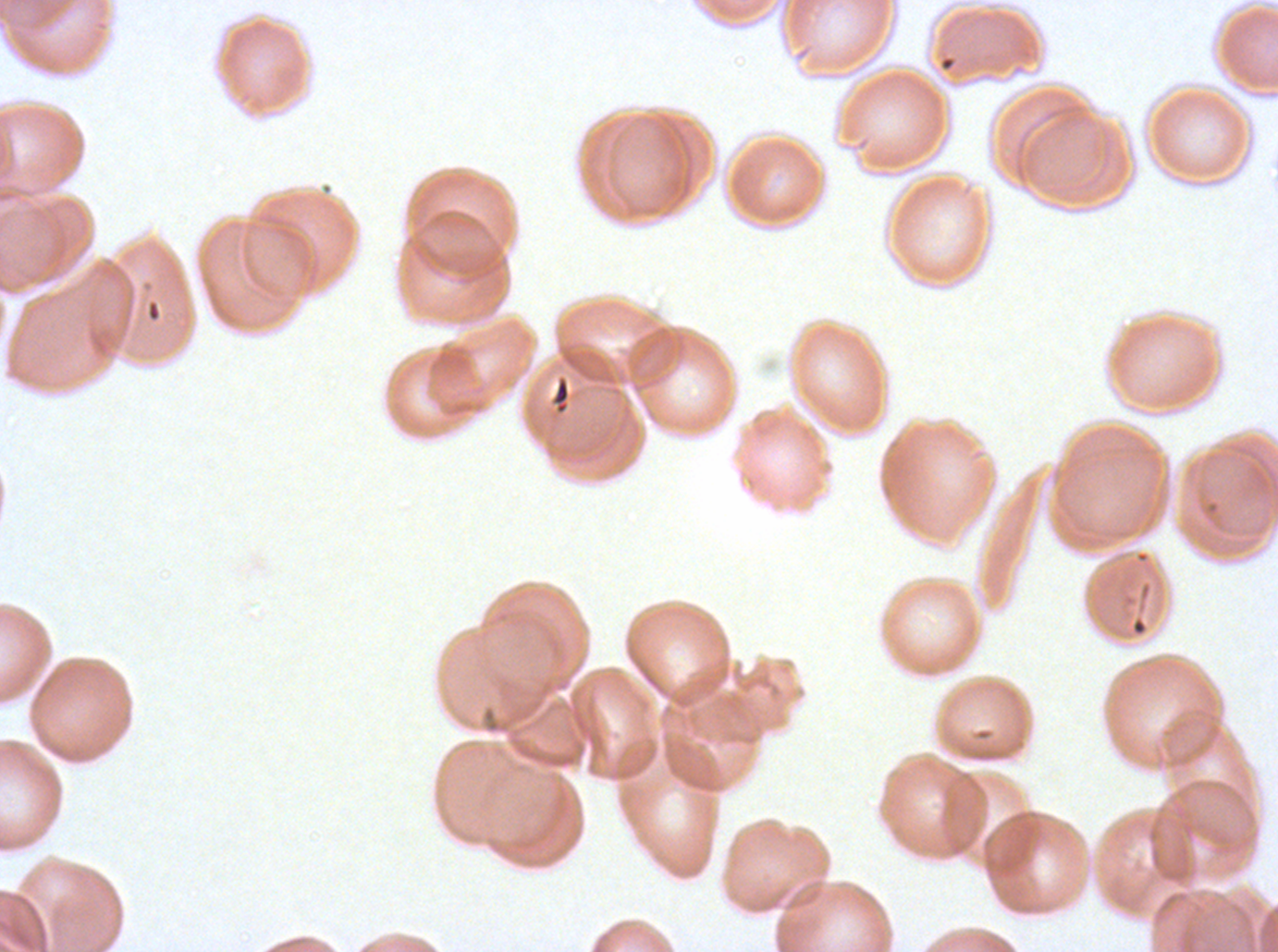

Approximate bounding boxes as {x1, y1, x2, y2} in pixels.
Summary:
  - Debris locations: {550, 375, 571, 415}, {1137, 580, 1153, 603}
  - Preparation: thin blood smear
  - Stain: Giemsa
  - Image size: 1278×952 pixels
  - Specimen: ex-vivo Plasmodium falciparum culture from a patient in The Gambia, grown for 24 to 48 hours
  - Field of view: sub-image separated from a larger composite